Assess this cell for malaria.
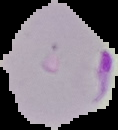

It is parasitized.

Segmented cell region on a black background. From a thin blood smear. Image is 118×130 pixels.